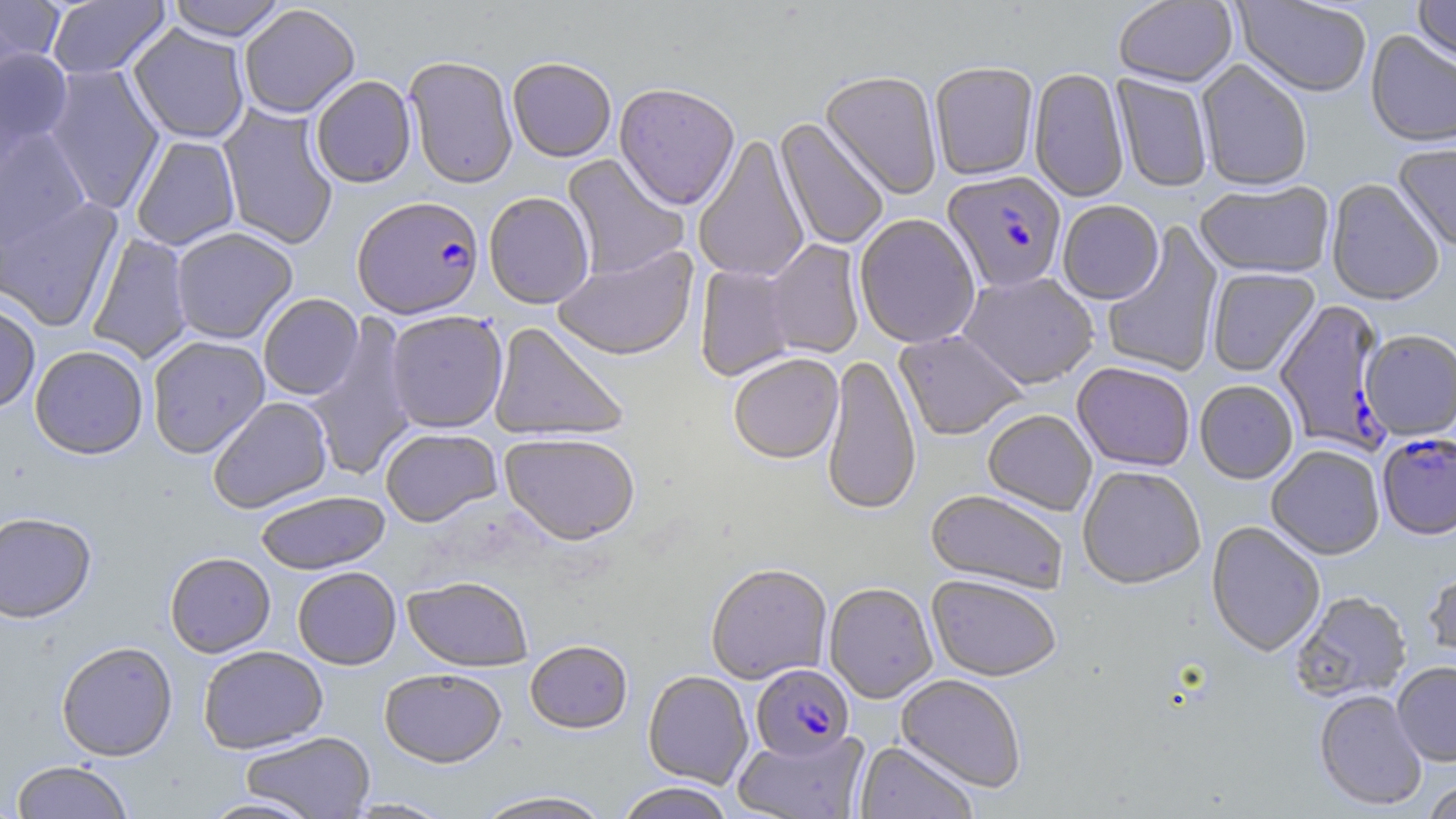

slide-level diagnosis = Plasmodium falciparum
field of view = single
Plasmodium falciparum-infected red blood cell locations = approximate bounding boxes as [x1, y1, x2, y2] in pixels: [942, 171, 1068, 294], [352, 196, 484, 318], [1274, 303, 1394, 455], [1377, 434, 1456, 542], [751, 664, 854, 761]
uninfected red blood cell locations = approximate bounding boxes as [x1, y1, x2, y2] in pixels: [0, 0, 66, 70], [46, 0, 170, 79], [166, 0, 288, 41], [1412, 0, 1456, 70], [1113, 1, 1237, 90], [1232, 1, 1373, 99], [238, 4, 360, 118], [128, 23, 250, 144], [1365, 31, 1456, 150], [0, 48, 74, 153], [404, 55, 518, 189], [507, 57, 616, 162], [1195, 60, 1312, 193], [929, 63, 1039, 182], [43, 64, 165, 214], [1028, 68, 1129, 204], [820, 72, 942, 200], [1110, 74, 1212, 193], [310, 75, 416, 188], [614, 84, 740, 212], [218, 105, 339, 249], [774, 119, 889, 251], [0, 127, 92, 251], [130, 135, 241, 251], [692, 135, 810, 283], [1392, 143, 1456, 253], [562, 154, 688, 281], [1326, 179, 1443, 308], [1195, 182, 1335, 281], [484, 191, 595, 309], [0, 195, 122, 330], [1057, 202, 1164, 306], [854, 215, 980, 350], [1102, 222, 1224, 377], [170, 227, 298, 344], [86, 230, 194, 364], [763, 240, 865, 360], [552, 244, 699, 361], [694, 263, 799, 381], [1207, 269, 1321, 379], [958, 273, 1100, 390], [258, 293, 363, 400], [0, 300, 40, 414], [385, 310, 508, 433], [305, 313, 418, 480], [488, 322, 629, 442], [893, 331, 1028, 442], [1360, 331, 1456, 441], [147, 335, 270, 458], [29, 344, 149, 459], [728, 354, 844, 465], [821, 354, 921, 517], [1072, 364, 1195, 473], [1195, 382, 1298, 485], [207, 396, 333, 513], [983, 411, 1097, 516], [380, 427, 502, 527], [499, 432, 640, 545], [1266, 447, 1385, 562], [1077, 467, 1205, 592], [254, 490, 390, 574], [926, 490, 1068, 595], [0, 511, 97, 623], [1206, 522, 1325, 659], [165, 551, 275, 657], [1423, 562, 1456, 668], [705, 563, 832, 684], [292, 567, 401, 669], [403, 576, 534, 672], [926, 576, 1062, 683], [824, 583, 938, 703], [1291, 592, 1412, 704], [56, 640, 178, 761], [525, 640, 633, 734], [198, 645, 328, 753], [1392, 663, 1456, 767], [379, 668, 507, 767], [643, 670, 754, 789], [895, 674, 1026, 793], [1314, 690, 1427, 812], [732, 729, 870, 819], [240, 731, 375, 818], [855, 741, 978, 819], [10, 760, 134, 818], [1422, 778, 1456, 819], [615, 783, 734, 819], [472, 790, 615, 819], [197, 795, 323, 818], [342, 797, 455, 818]
magnification = 1000x
stain = May-Grünwald-Giemsa
preparation = thin blood smear
image size = 1456×819 pixels
modality = light microscopy